Classify this cell by malaria status.
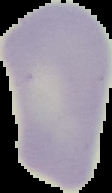

Uninfected.

preparation = thin blood smear
image size = 112×193 pixels
image type = segmented cell region with the area outside set to black